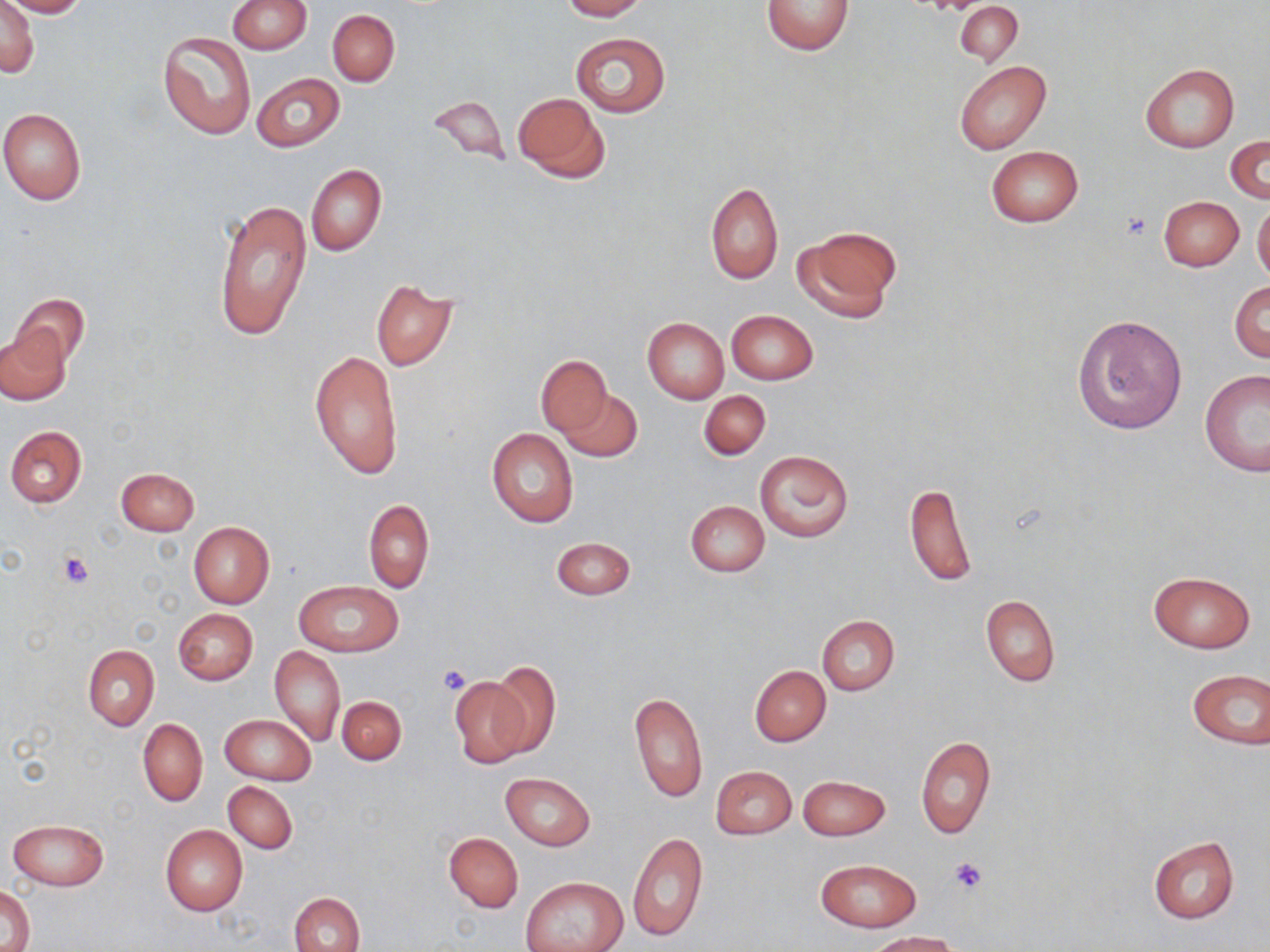

{
  "slide_level_diagnosis": "no evidence of blood parasites",
  "preparation": "thin blood smear",
  "stain": "May-Grünwald-Giemsa",
  "magnification": "1000x",
  "platelet_locations": "approximate bounding boxes as named x1/y1/x2/y2 corners in pixels: (x1=1123, y1=211, x2=1152, y2=242), (x1=57, y1=550, x2=94, y2=589), (x1=437, y1=664, x2=472, y2=695), (x1=949, y1=857, x2=989, y2=894)",
  "modality": "light microscopy",
  "uninfected_red_blood_cell_locations": "approximate bounding boxes as named x1/y1/x2/y2 corners in pixels: (x1=0, y1=0, x2=39, y2=78), (x1=1, y1=0, x2=88, y2=18), (x1=228, y1=0, x2=311, y2=54), (x1=561, y1=0, x2=646, y2=20), (x1=761, y1=0, x2=857, y2=55), (x1=955, y1=2, x2=1022, y2=65), (x1=327, y1=9, x2=399, y2=86), (x1=157, y1=31, x2=255, y2=139), (x1=571, y1=32, x2=670, y2=117), (x1=954, y1=60, x2=1052, y2=155), (x1=1139, y1=62, x2=1238, y2=152), (x1=251, y1=72, x2=344, y2=152), (x1=513, y1=91, x2=610, y2=182), (x1=429, y1=93, x2=510, y2=167), (x1=0, y1=109, x2=86, y2=204), (x1=1226, y1=135, x2=1269, y2=204), (x1=986, y1=145, x2=1084, y2=228), (x1=306, y1=164, x2=385, y2=256), (x1=704, y1=182, x2=783, y2=284), (x1=1159, y1=196, x2=1244, y2=271), (x1=212, y1=197, x2=312, y2=344), (x1=1252, y1=197, x2=1270, y2=285), (x1=794, y1=226, x2=902, y2=323), (x1=370, y1=280, x2=457, y2=371), (x1=1229, y1=280, x2=1270, y2=363), (x1=9, y1=293, x2=91, y2=371), (x1=726, y1=310, x2=817, y2=384), (x1=1073, y1=313, x2=1189, y2=435), (x1=643, y1=317, x2=729, y2=404), (x1=1, y1=325, x2=70, y2=404), (x1=309, y1=349, x2=404, y2=481), (x1=535, y1=356, x2=612, y2=433), (x1=1200, y1=369, x2=1270, y2=476), (x1=556, y1=386, x2=641, y2=460), (x1=698, y1=390, x2=770, y2=460), (x1=4, y1=425, x2=86, y2=508), (x1=486, y1=428, x2=579, y2=530), (x1=755, y1=450, x2=854, y2=542), (x1=115, y1=467, x2=200, y2=536), (x1=903, y1=483, x2=976, y2=588), (x1=363, y1=498, x2=433, y2=592), (x1=685, y1=499, x2=770, y2=577), (x1=187, y1=521, x2=275, y2=608), (x1=550, y1=537, x2=636, y2=600), (x1=1147, y1=570, x2=1255, y2=653), (x1=294, y1=580, x2=402, y2=656), (x1=981, y1=594, x2=1060, y2=687), (x1=174, y1=608, x2=258, y2=684), (x1=817, y1=616, x2=900, y2=694), (x1=82, y1=644, x2=158, y2=730), (x1=270, y1=646, x2=345, y2=745), (x1=484, y1=662, x2=561, y2=761), (x1=750, y1=665, x2=831, y2=746), (x1=1185, y1=667, x2=1269, y2=751), (x1=450, y1=672, x2=533, y2=768), (x1=630, y1=691, x2=708, y2=804), (x1=337, y1=695, x2=406, y2=765), (x1=220, y1=714, x2=317, y2=785), (x1=137, y1=718, x2=208, y2=806), (x1=916, y1=735, x2=995, y2=839), (x1=711, y1=765, x2=797, y2=840), (x1=500, y1=772, x2=596, y2=851), (x1=798, y1=775, x2=890, y2=840), (x1=223, y1=782, x2=297, y2=854), (x1=8, y1=818, x2=108, y2=890), (x1=160, y1=824, x2=248, y2=915), (x1=628, y1=830, x2=707, y2=942), (x1=444, y1=831, x2=523, y2=913), (x1=1148, y1=837, x2=1239, y2=924), (x1=815, y1=858, x2=920, y2=932), (x1=522, y1=877, x2=625, y2=952), (x1=2, y1=884, x2=33, y2=952), (x1=290, y1=891, x2=365, y2=952), (x1=865, y1=931, x2=962, y2=952)",
  "image_size": "1270×952 pixels",
  "field_of_view": "single"
}